Comment on the morphology of the red blood cells.
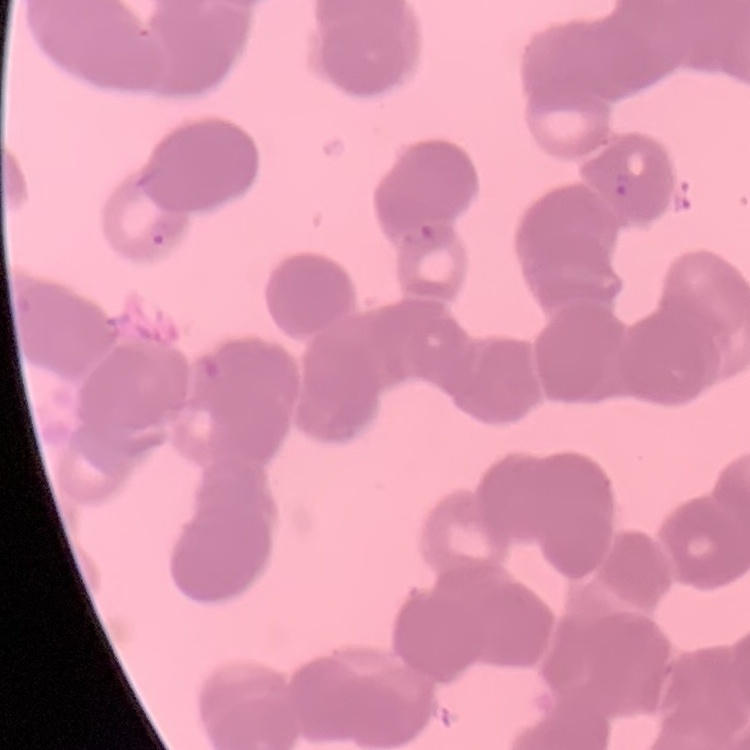
They show rouleaux formation.

One tile cut from a larger photomicrograph. Field's or Giemsa stain. Thin blood film.